Comment on the morphology of the erythrocytes.
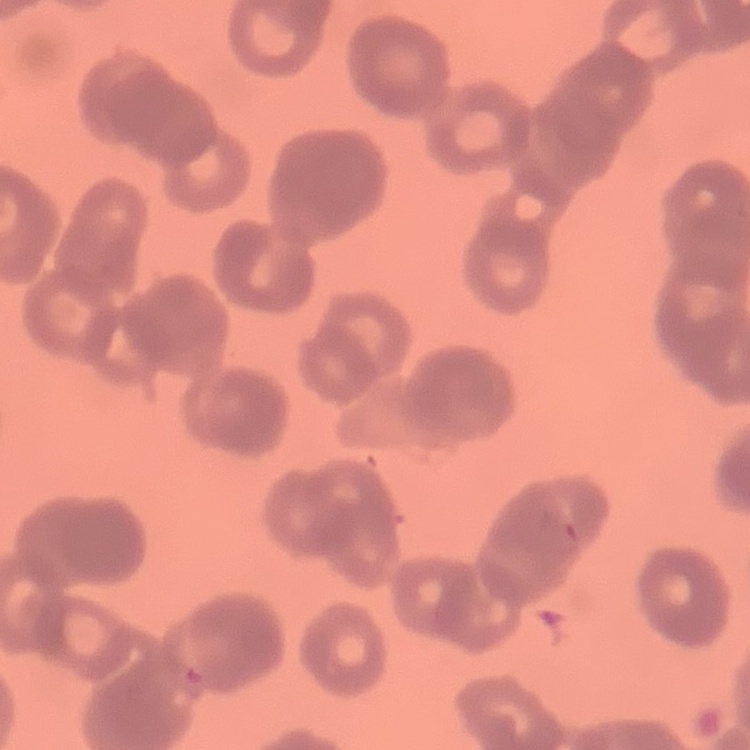
Rouleaux formation.

image type = one tile cut from a larger photomicrograph
preparation = thin peripheral smear
stain = Field's or Giemsa